Classify this cell by malaria status.
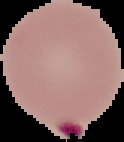

It is parasitized.

Summary:
  - Image type: segmented cell region on a black background
  - Preparation: thin blood smear
  - Image size: 124×142 pixels